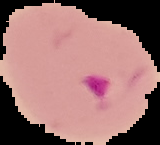
preparation = thin blood film
image type = cell region segmented out of the field of view; surrounding area masked to black
malaria status = parasitized
image size = 160×145 pixels